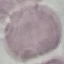

malaria status = uninfected
preparation = thin blood smear
image type = automatically extracted cell patch, resized to 64 × 64 pixels
capture = smartphone through the microscope eyepiece
stain = Giemsa